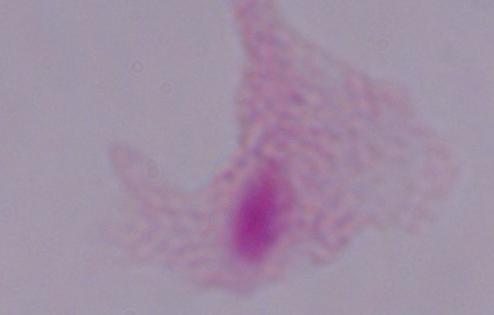

Summary:
  - Identification: trichomonad
  - Magnification: 1000x
  - Modality: micrograph